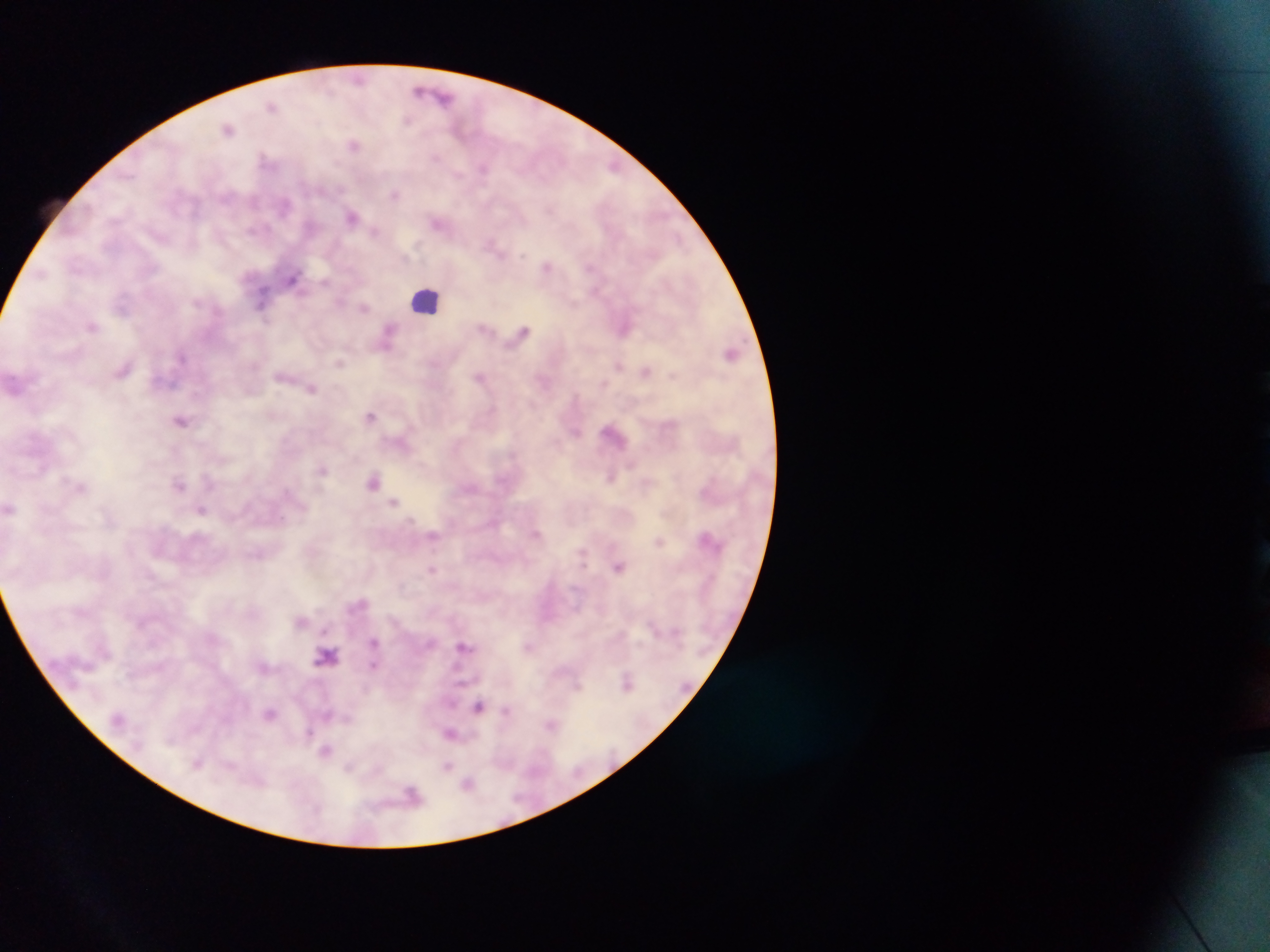

field_of_view: single
malaria_parasite_locations: 'approximate centers as (x, y) in pixels: (358, 78), (419, 91), (445, 97), (272, 106), (406, 119), (229, 128), (354, 145), (264, 157), (436, 158), (613, 165), (484, 168), (458, 175), (395, 194), (284, 205), (551, 209), (351, 216), (437, 223), (374, 231), (492, 244), (522, 256), (547, 266), (589, 267), (42, 273), (293, 278), (325, 282), (262, 299), (339, 302), (364, 308), (92, 326), (484, 327), (523, 329), (625, 329), (390, 331), (386, 346), (182, 356), (340, 362), (617, 366), (124, 369), (646, 370), (673, 376), (280, 377), (480, 377), (311, 389), (371, 416), (181, 420), (576, 433), (323, 470), (610, 478), (208, 479), (374, 481), (179, 485), (394, 501), (202, 509), (535, 534), (434, 535), (658, 541), (257, 555), (618, 568), (433, 569), (301, 621), (325, 631), (373, 641), (463, 646), (327, 655), (374, 665), (627, 683), (578, 686), (478, 706), (506, 710), (270, 713), (328, 715), (347, 718), (552, 726), (308, 733), (450, 733), (326, 751), (198, 763), (349, 766), (447, 766), (469, 783), (412, 794)'
leukocyte_locations: 'approximate centers as (x, y) in pixels: (425, 300)'
image_size: 1270×952 pixels
country: Ghana
preparation: thick blood film
capture: mobile-phone photograph through a microscope